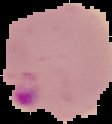
Image is 112×124 pixels. Malaria status: parasitized. Segmented cell region on a black background. From a thin blood film.